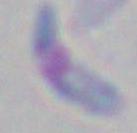

{
  "identification": "Toxoplasma gondii",
  "magnification": "1000x",
  "modality": "photomicrograph"
}